Name the parasite shown.
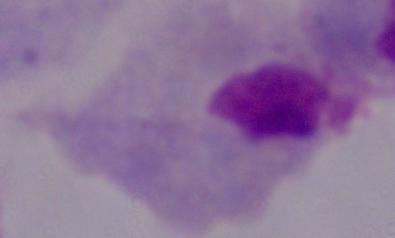
This is a trichomonad.

Micrograph. Captured at 1000x magnification.